Give the extent of all uninfected red blood cells.
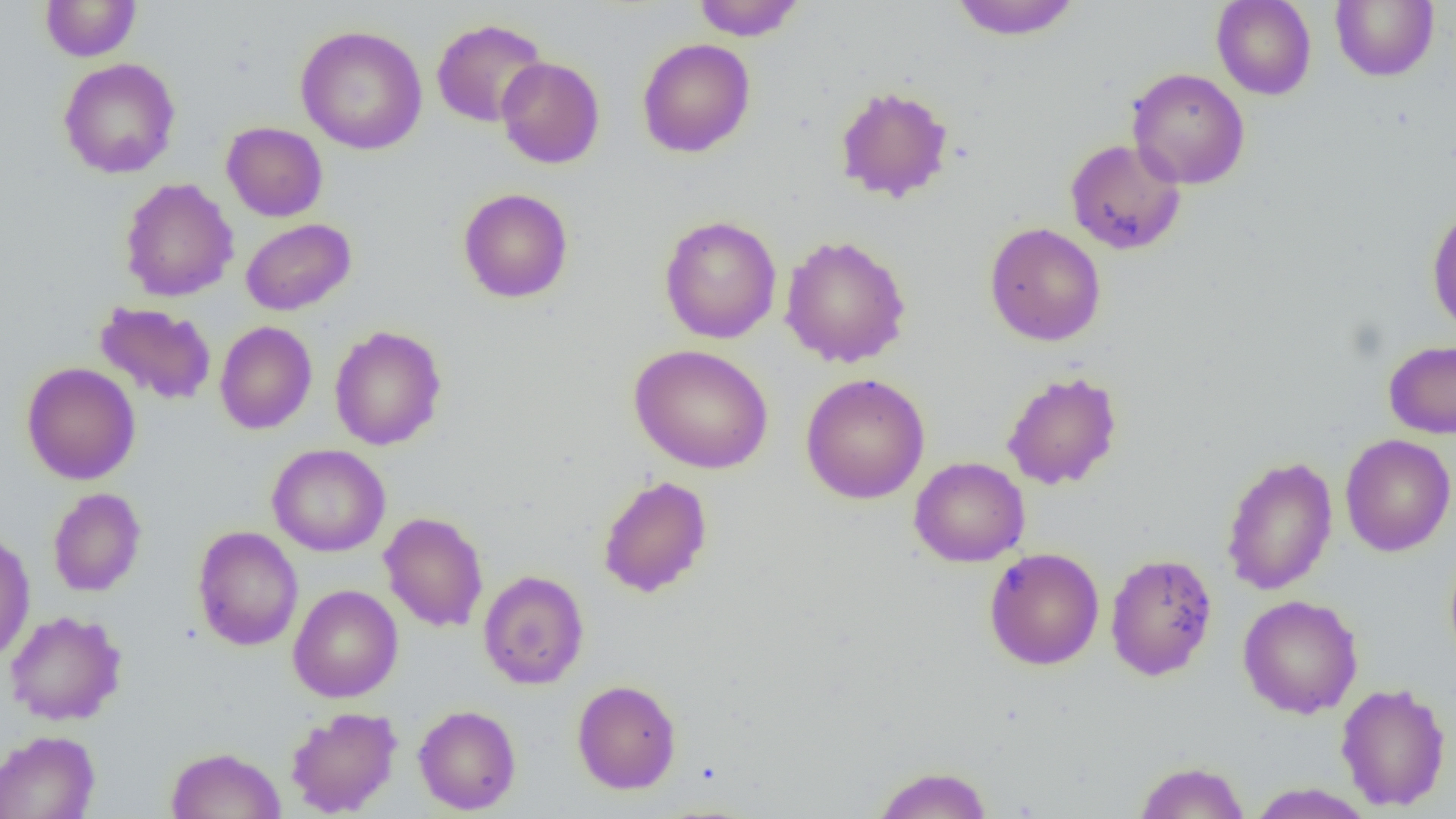

Approximate bounding boxes as [x1, y1, x2, y2] in pixels.
Uninfected red blood cells: [692, 0, 805, 41], [948, 0, 1083, 41], [1211, 0, 1317, 100], [39, 1, 141, 62], [1331, 1, 1439, 81], [431, 18, 549, 127], [295, 25, 428, 155], [637, 38, 755, 158], [496, 56, 605, 169], [58, 58, 180, 179], [1127, 68, 1250, 189], [834, 85, 955, 204], [221, 122, 328, 222], [1065, 138, 1186, 255], [119, 177, 238, 302], [457, 188, 574, 303], [1426, 202, 1456, 334], [659, 215, 782, 343], [241, 218, 356, 315], [985, 221, 1106, 346], [792, 231, 916, 503], [779, 234, 912, 368], [94, 302, 217, 406], [214, 321, 317, 435], [329, 325, 447, 451], [1383, 339, 1456, 439], [629, 344, 774, 474], [21, 361, 141, 485], [1002, 371, 1123, 491], [800, 373, 930, 504], [1340, 433, 1456, 557], [267, 444, 391, 556], [1220, 455, 1338, 595], [909, 457, 1030, 567], [597, 475, 713, 598], [47, 487, 147, 597], [379, 512, 489, 633], [192, 525, 304, 651], [0, 528, 36, 663], [984, 547, 1105, 670], [1105, 552, 1217, 681], [478, 570, 589, 689], [287, 584, 403, 703], [1237, 594, 1363, 718], [5, 610, 127, 726], [572, 679, 682, 794], [1335, 681, 1451, 812], [413, 705, 521, 815], [285, 706, 402, 817], [0, 730, 100, 819], [166, 747, 286, 819], [1132, 760, 1250, 818], [871, 765, 993, 819], [1246, 783, 1376, 818].

Summary:
  - Slide-level diagnosis: negative for blood parasites
  - Preparation: thin blood film
  - Field of view: one of a larger specimen
  - Image size: 1456×819 pixels
  - Modality: light microscopy
  - Magnification: 1000x